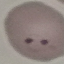 Malaria status: parasitized. Giemsa-stained preparation. Acquired by smartphone through the microscope eyepiece. Thin blood film. Cell patch, automatically extracted from a larger field of view and resized to 64 × 64 pixels.